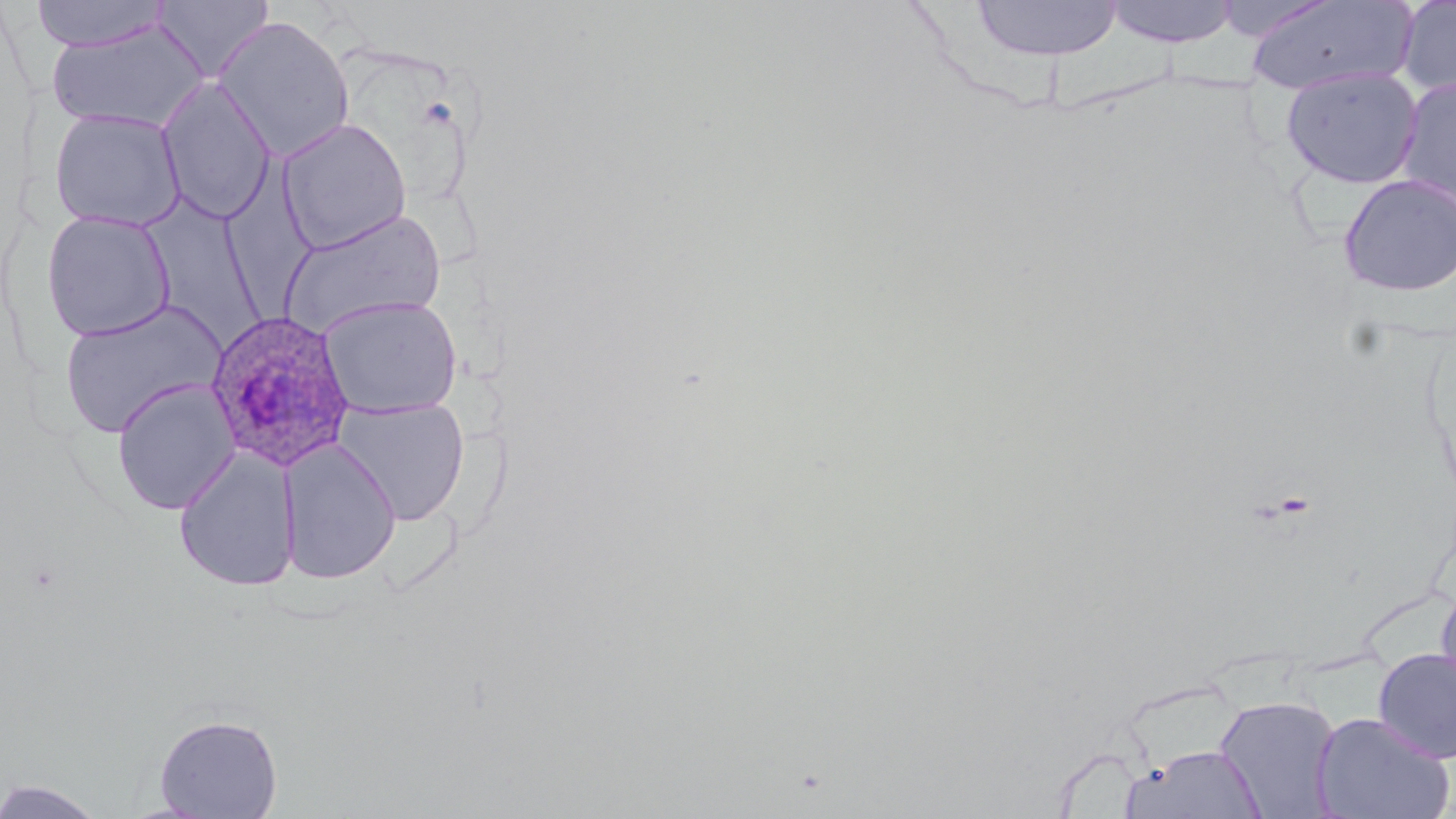
Plasmodium ovale-infected red blood cell locations = approximate bounding boxes as (x1,y1)-(x2,y2) corner pairs in pixels: (205,310)-(357,471)
slide-level diagnosis = Plasmodium ovale
image size = 1456×819 pixels
magnification = 1000x
modality = light microscopy
preparation = thin blood film
field of view = single
stain = May-Grünwald-Giemsa
uninfected red blood cell locations = approximate bounding boxes as (x1,y1)-(x2,y2) corner pairs in pixels: (151,0)-(275,82), (970,0)-(1123,61), (1103,0)-(1241,48), (1243,0)-(1419,96), (1396,0)-(1456,101), (31,1)-(170,52), (213,15)-(355,161), (46,20)-(207,133), (1280,66)-(1424,189), (156,77)-(277,226), (1395,77)-(1456,216), (48,108)-(187,233), (276,117)-(412,253), (220,151)-(322,330), (1338,173)-(1456,297), (146,198)-(267,356), (278,208)-(447,338), (40,210)-(176,342), (318,295)-(464,418), (56,298)-(227,439), (111,378)-(240,515), (333,397)-(470,526), (279,438)-(401,585), (173,446)-(301,592), (1435,578)-(1456,713), (1373,647)-(1456,763), (1214,694)-(1342,818), (1311,711)-(1454,819), (154,713)-(283,818), (1123,744)-(1268,818), (1,777)-(107,819)